Locate every malaria parasite.
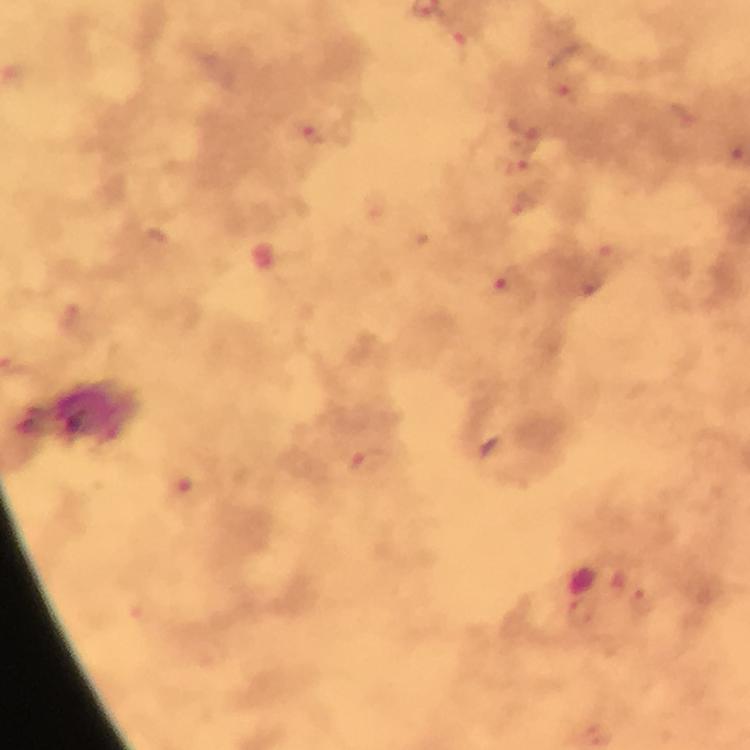
Approximate centers as (x, y) in pixels.
Malaria parasites: (464, 46), (563, 93), (309, 132), (523, 132), (735, 154), (522, 171), (523, 205), (609, 254), (509, 285), (590, 286), (366, 463), (185, 492), (640, 603), (581, 612).

Summary:
  - Context: from a diagnostic examination for malaria
  - Stain: Giemsa
  - Preparation: thick blood film
  - Immersion oil: applied
  - Capture: smartphone photograph through a microscope
  - Cropped from: a single field of view
  - Magnification: 100x
  - Image size: 750×750 pixels